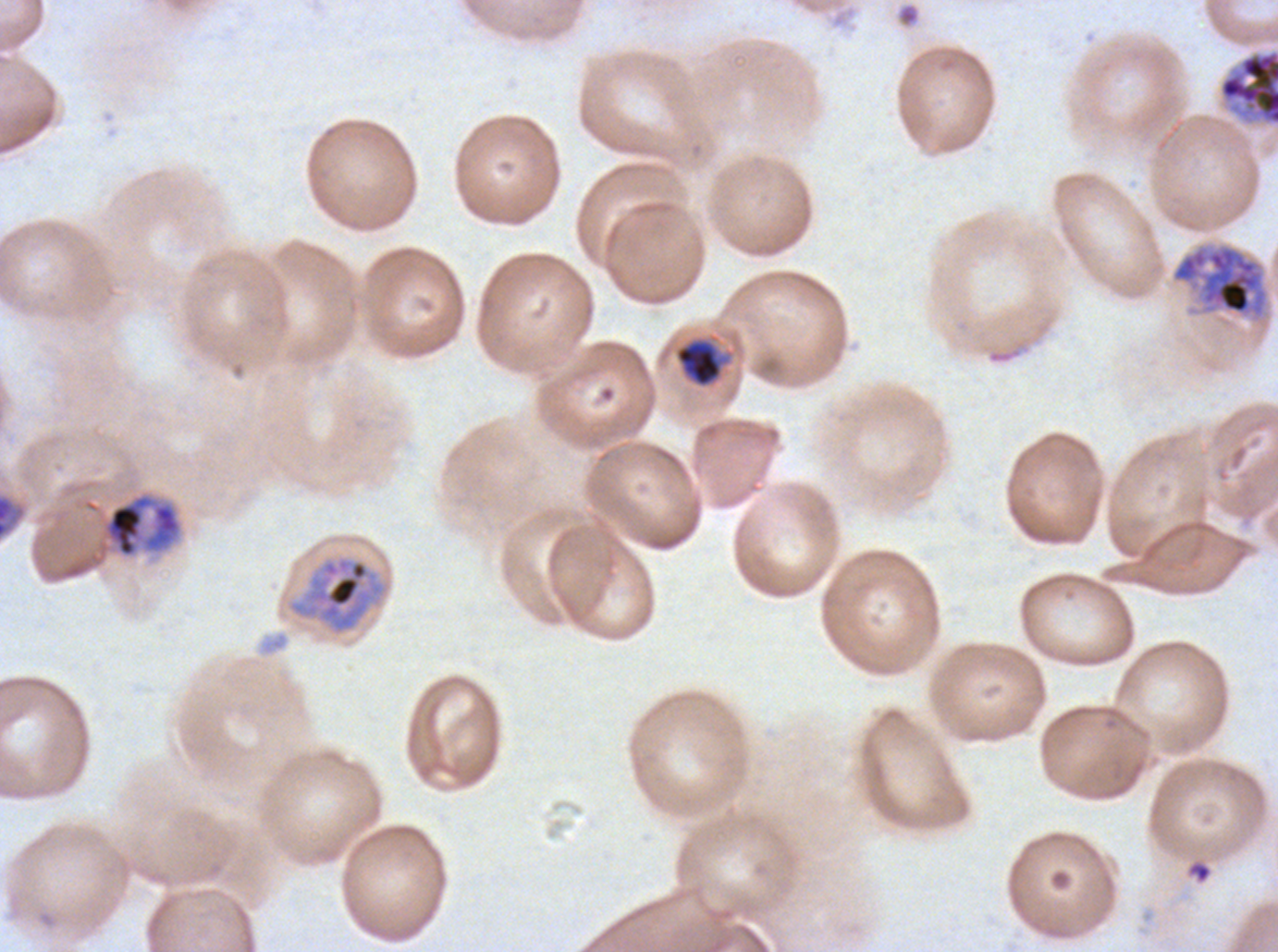

Approximate bounding rectangles given as corner coordinates in pixels from the top-left.
Summary:
  - Late trophozoite locations: (x1=102, y1=493, x2=182, y2=558)
  - Early schizont locations: (x1=1171, y1=244, x2=1269, y2=319), (x1=288, y1=555, x2=387, y2=636)
  - Late-ring/early-trophozoite locations: (x1=674, y1=338, x2=723, y2=388)
  - Debris locations: (x1=1188, y1=861, x2=1211, y2=884)
  - Segmenter locations: (x1=1218, y1=48, x2=1277, y2=127)
  - Preparation: thin blood film
  - Life-cycle stages observed: late-ring/early-trophozoite, late trophozoite, early schizont, segmenter
  - Stain: Giemsa
  - Image size: 1278×952 pixels
  - Specimen: Plasmodium falciparum from a patient in The Gambia, cultured ex vivo for 24 to 48 hours
  - Field of view: sub-image separated from a larger composite